State which parasite is depicted.
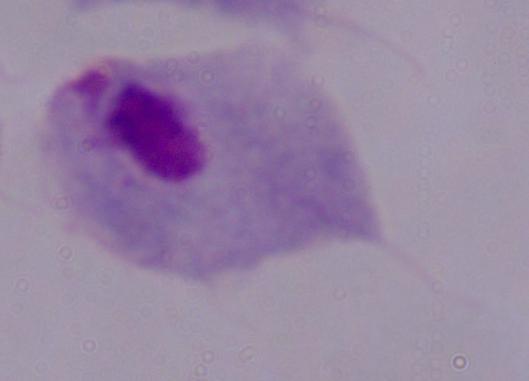

This is a trichomonad.

1000x magnification. Micrograph.